Identify the preparation type.
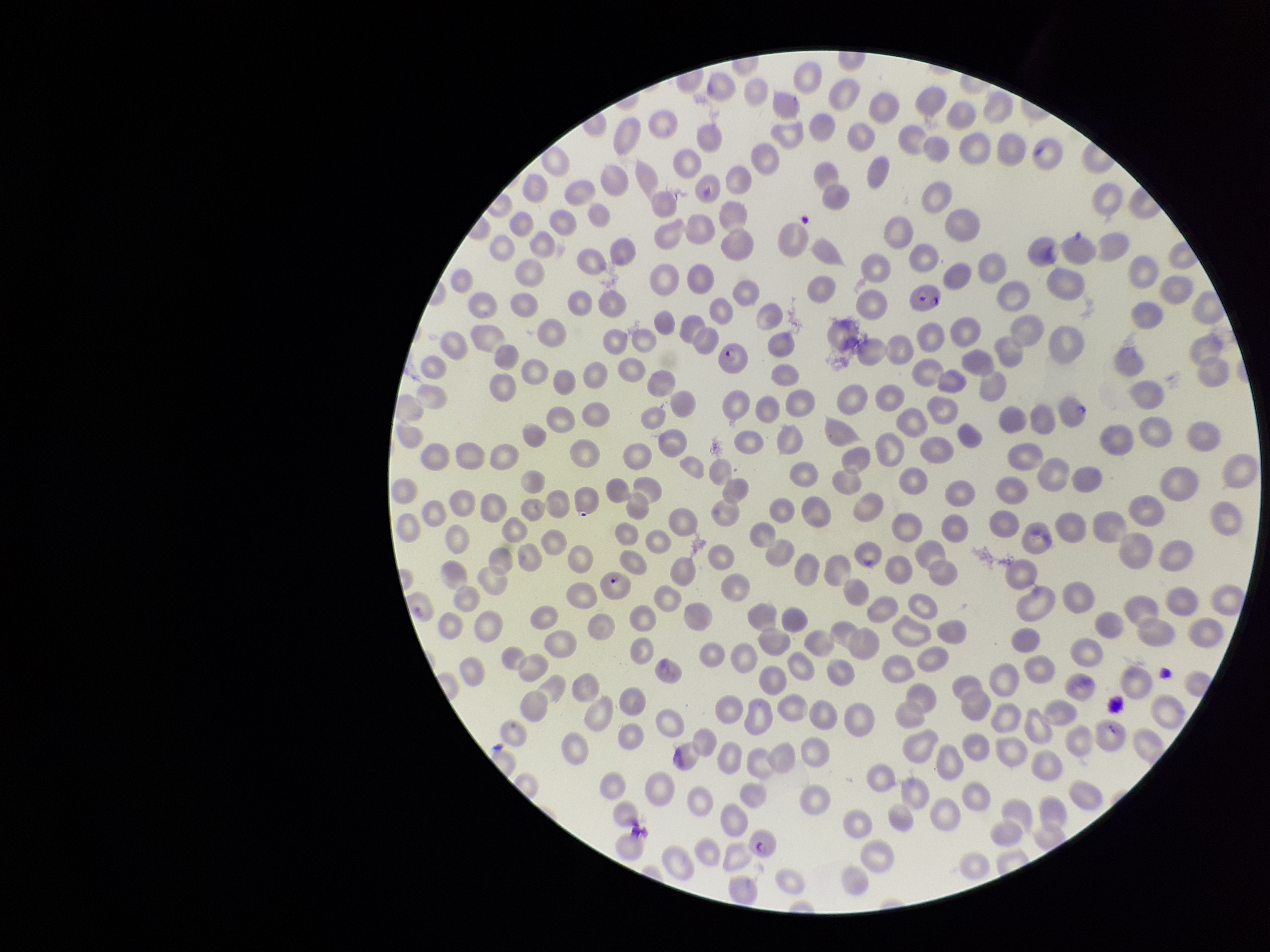

A thin smear.

Giemsa stain. Single field of view. Photographed through the microscope eyepiece with a smartphone camera. Species reported for this patient: Plasmodium falciparum. Parasitized red blood cell count: 5. Patient malaria status: infected. Image is 1270×952 pixels. Parasitized red blood cells: detected. Red blood cell count: 306.